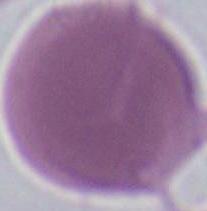

magnification = 1000x
identification = red blood cell
modality = photomicrograph